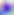
identification: Toxoplasma gondii
magnification: 400x
modality: photomicrograph